Assess this cell for malaria.
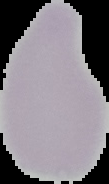
Uninfected.

Summary:
  - Image type: segmented cell region with the area outside set to black
  - Preparation: thin blood film
  - Image size: 109×184 pixels